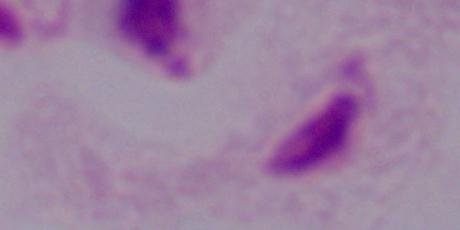

Captured at 1000x magnification. A trichomonad is shown. Micrograph.